Assess this cell for malaria.
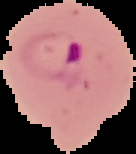
It is parasitized.

Summary:
  - Image size: 136×154 pixels
  - Image type: cell region segmented out of the field of view; surrounding area masked to black
  - Preparation: thin blood smear